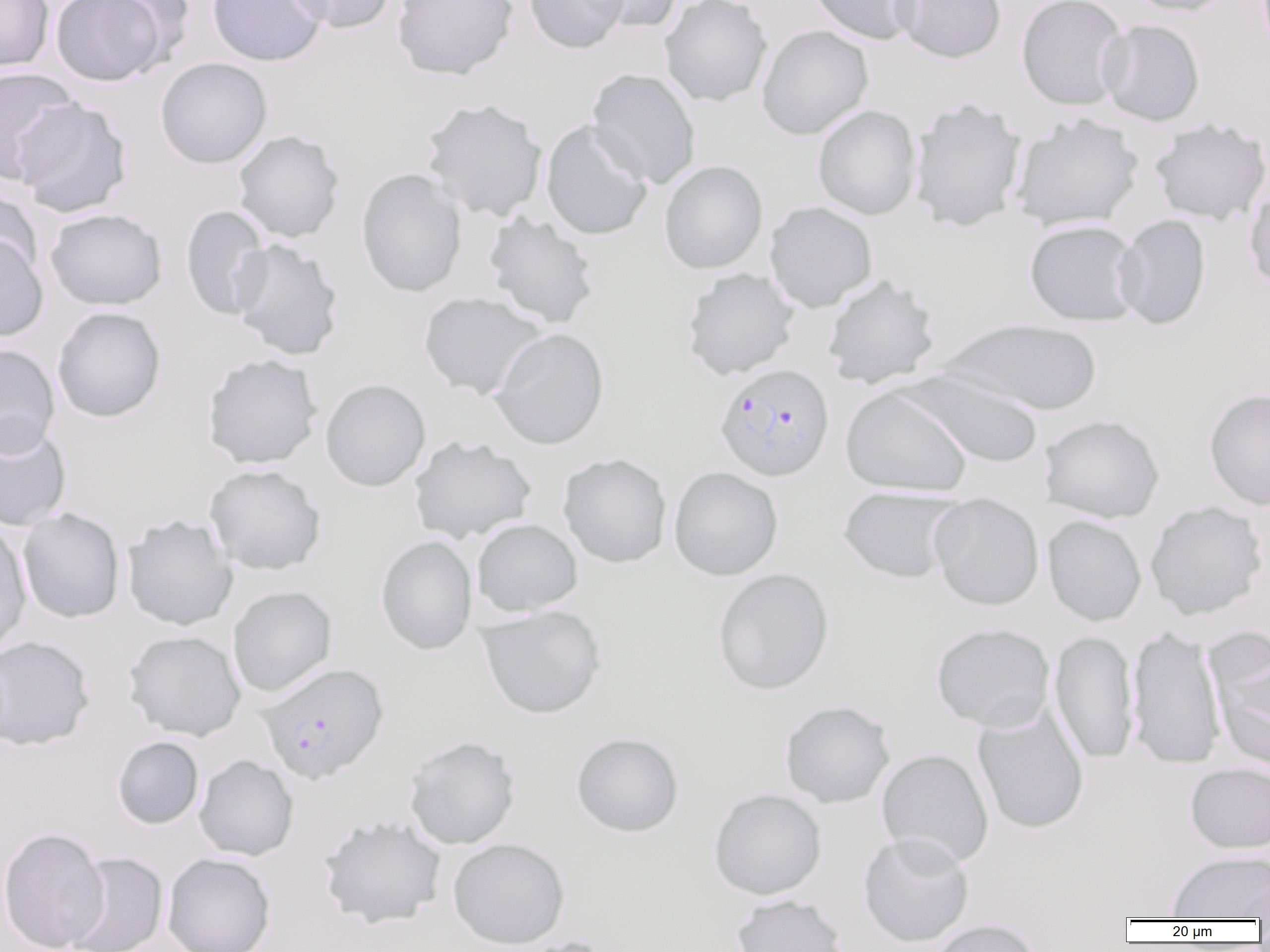

slide-level diagnosis = Plasmodium falciparum
magnification = 1000x
image size = 1270×952 pixels
uninfected red blood cell locations = approximate bounding boxes as named x1/y1/x2/y2 corners in pixels: (x1=0, y1=0, x2=54, y2=73), (x1=50, y1=0, x2=167, y2=86), (x1=92, y1=0, x2=197, y2=69), (x1=207, y1=0, x2=328, y2=67), (x1=286, y1=0, x2=397, y2=34), (x1=392, y1=0, x2=518, y2=80), (x1=524, y1=0, x2=629, y2=54), (x1=585, y1=0, x2=683, y2=34), (x1=659, y1=0, x2=772, y2=107), (x1=807, y1=0, x2=922, y2=45), (x1=890, y1=0, x2=1007, y2=63), (x1=1125, y1=0, x2=1236, y2=17), (x1=1016, y1=1, x2=1130, y2=110), (x1=1098, y1=19, x2=1205, y2=126), (x1=756, y1=24, x2=873, y2=140), (x1=155, y1=57, x2=272, y2=169), (x1=0, y1=67, x2=82, y2=183), (x1=587, y1=68, x2=701, y2=190), (x1=421, y1=97, x2=547, y2=222), (x1=908, y1=97, x2=1027, y2=232), (x1=12, y1=98, x2=132, y2=217), (x1=813, y1=105, x2=921, y2=220), (x1=1009, y1=113, x2=1143, y2=231), (x1=1149, y1=118, x2=1270, y2=225), (x1=540, y1=119, x2=654, y2=241), (x1=232, y1=129, x2=345, y2=243), (x1=659, y1=160, x2=767, y2=274), (x1=356, y1=168, x2=467, y2=298), (x1=1244, y1=180, x2=1270, y2=293), (x1=0, y1=188, x2=43, y2=285), (x1=764, y1=202, x2=878, y2=313), (x1=180, y1=205, x2=273, y2=321), (x1=45, y1=208, x2=167, y2=311), (x1=483, y1=211, x2=600, y2=329), (x1=1114, y1=214, x2=1211, y2=330), (x1=1024, y1=219, x2=1142, y2=326), (x1=0, y1=233, x2=48, y2=342), (x1=229, y1=239, x2=344, y2=361), (x1=681, y1=267, x2=800, y2=380), (x1=822, y1=274, x2=940, y2=390), (x1=418, y1=291, x2=546, y2=400), (x1=52, y1=306, x2=166, y2=422), (x1=937, y1=318, x2=1104, y2=416), (x1=489, y1=328, x2=609, y2=449), (x1=0, y1=344, x2=60, y2=456), (x1=202, y1=353, x2=322, y2=469), (x1=900, y1=369, x2=1046, y2=469), (x1=320, y1=378, x2=431, y2=492), (x1=840, y1=386, x2=973, y2=496), (x1=1203, y1=387, x2=1270, y2=510), (x1=1039, y1=414, x2=1164, y2=522), (x1=0, y1=418, x2=72, y2=532), (x1=408, y1=436, x2=536, y2=543), (x1=558, y1=453, x2=672, y2=568), (x1=204, y1=464, x2=326, y2=575), (x1=669, y1=466, x2=783, y2=581), (x1=838, y1=486, x2=964, y2=584), (x1=928, y1=493, x2=1044, y2=610), (x1=1144, y1=501, x2=1268, y2=620), (x1=18, y1=508, x2=125, y2=624), (x1=122, y1=514, x2=238, y2=631), (x1=1042, y1=515, x2=1146, y2=626), (x1=472, y1=518, x2=583, y2=616), (x1=0, y1=521, x2=31, y2=654), (x1=375, y1=536, x2=478, y2=655), (x1=712, y1=567, x2=834, y2=695), (x1=227, y1=585, x2=337, y2=697), (x1=476, y1=605, x2=606, y2=719), (x1=931, y1=623, x2=1055, y2=732), (x1=1126, y1=626, x2=1227, y2=769), (x1=123, y1=630, x2=246, y2=741), (x1=1049, y1=631, x2=1139, y2=764), (x1=0, y1=635, x2=95, y2=751), (x1=1211, y1=648, x2=1270, y2=772), (x1=780, y1=700, x2=895, y2=808), (x1=972, y1=706, x2=1089, y2=835), (x1=571, y1=732, x2=684, y2=837), (x1=404, y1=735, x2=520, y2=850), (x1=111, y1=736, x2=204, y2=830), (x1=876, y1=748, x2=994, y2=868), (x1=194, y1=755, x2=299, y2=861), (x1=1185, y1=763, x2=1270, y2=853), (x1=708, y1=788, x2=827, y2=900), (x1=317, y1=814, x2=448, y2=929), (x1=0, y1=827, x2=109, y2=952), (x1=858, y1=831, x2=975, y2=947), (x1=448, y1=838, x2=569, y2=948), (x1=63, y1=851, x2=168, y2=952), (x1=1167, y1=851, x2=1270, y2=920), (x1=163, y1=853, x2=276, y2=952), (x1=1234, y1=880, x2=1270, y2=920), (x1=731, y1=893, x2=849, y2=952), (x1=930, y1=919, x2=1044, y2=952)
preparation = thin blood film
field of view = one of a larger specimen
modality = optical microscopy
Plasmodium falciparum-infected red blood cell locations = approximate bounding boxes as named x1/y1/x2/y2 corners in pixels: (x1=713, y1=363, x2=834, y2=481), (x1=258, y1=663, x2=388, y2=784)